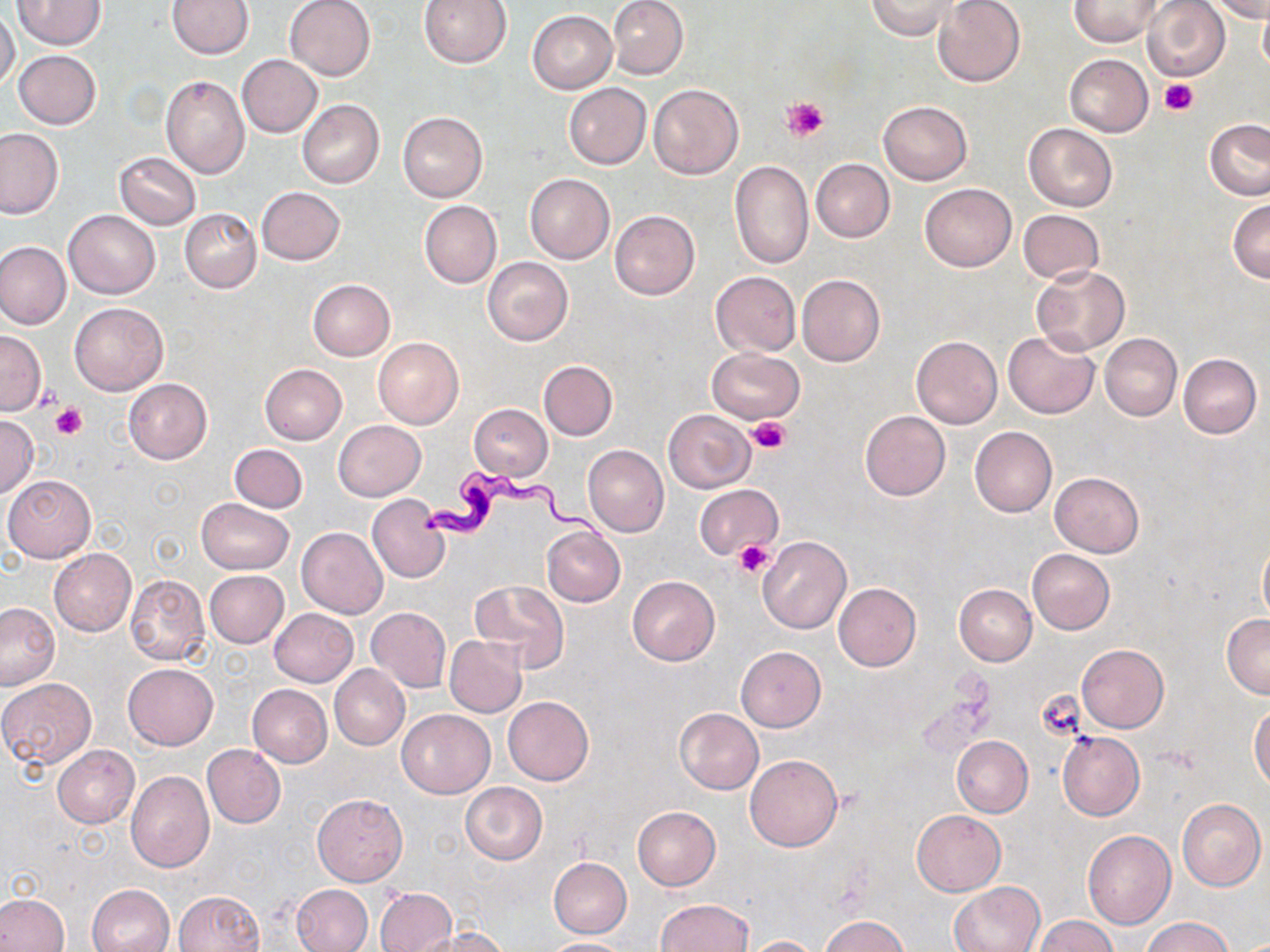

slide-level diagnosis = Trypanosoma brucei
platelet locations = approximate bounding boxes as (x1, y1, x2, y2) in pixels: (1159, 77, 1197, 117), (782, 97, 829, 141), (34, 383, 63, 412), (51, 405, 87, 440), (747, 418, 789, 453), (733, 541, 776, 578), (1036, 689, 1085, 741)
image size = 1270×952 pixels
modality = light microscopy
Trypanosoma brucei locations = approximate bounding boxes as (x1, y1, x2, y2) in pixels: (420, 468, 615, 549)
magnification = 1000x
preparation = thin blood film
stain = May-Grünwald-Giemsa
uninfected red blood cell locations = approximate bounding boxes as (x1, y1, x2, y2) in pixels: (12, 0, 104, 49), (168, 0, 254, 58), (284, 0, 376, 81), (417, 0, 512, 68), (607, 0, 688, 80), (866, 0, 958, 39), (1069, 0, 1165, 46), (1212, 0, 1270, 22), (933, 1, 1025, 88), (1142, 1, 1230, 82), (0, 8, 20, 91), (1258, 8, 1270, 75), (527, 10, 617, 94), (13, 50, 102, 129), (1064, 53, 1154, 136), (236, 55, 323, 137), (160, 75, 249, 178), (647, 82, 744, 179), (564, 83, 651, 169), (297, 99, 384, 188), (879, 100, 971, 184), (397, 111, 488, 201), (1205, 119, 1270, 198), (1023, 123, 1117, 211), (0, 129, 63, 218), (114, 151, 201, 230), (729, 159, 813, 269), (811, 159, 895, 243), (525, 173, 615, 263), (919, 182, 1017, 272), (256, 186, 344, 264), (419, 200, 502, 288), (1228, 200, 1270, 283), (180, 208, 261, 293), (63, 210, 159, 298), (610, 210, 699, 300), (1018, 210, 1105, 284), (0, 241, 72, 329), (482, 256, 573, 346), (1032, 265, 1129, 355), (710, 271, 801, 356), (796, 274, 885, 368), (308, 279, 394, 361), (69, 301, 168, 396), (0, 330, 45, 414), (1003, 331, 1100, 419), (1100, 333, 1181, 421), (911, 335, 1002, 429), (373, 337, 463, 430), (706, 348, 805, 424), (1178, 353, 1262, 438), (539, 361, 617, 440), (260, 364, 347, 444), (123, 377, 212, 464), (468, 404, 552, 480), (663, 408, 755, 493), (860, 411, 950, 500), (0, 416, 39, 497), (334, 420, 425, 500), (970, 426, 1056, 517), (229, 443, 307, 512), (582, 444, 668, 538), (1050, 471, 1144, 556), (2, 475, 95, 562), (693, 483, 782, 562), (367, 494, 450, 583), (196, 498, 292, 573), (297, 527, 389, 619), (541, 527, 625, 606), (757, 536, 851, 633), (1258, 539, 1270, 626), (49, 548, 135, 636), (1027, 549, 1114, 634), (204, 570, 289, 647), (124, 574, 209, 665), (627, 576, 719, 665), (472, 578, 569, 672), (833, 583, 921, 671), (954, 583, 1037, 665), (0, 602, 59, 692), (366, 607, 451, 692), (270, 608, 357, 686), (1222, 614, 1270, 698), (444, 636, 527, 717), (1077, 644, 1168, 732), (735, 646, 827, 732), (123, 663, 218, 750), (330, 664, 409, 749), (0, 677, 97, 769), (248, 684, 333, 767), (503, 695, 593, 786), (1249, 704, 1270, 790), (674, 707, 764, 794), (396, 710, 495, 798), (1056, 730, 1143, 820), (952, 735, 1033, 818), (202, 743, 286, 828), (52, 745, 140, 828), (744, 755, 842, 852), (126, 771, 213, 872), (460, 782, 547, 864), (312, 793, 408, 886), (1176, 799, 1266, 891), (633, 806, 720, 890), (911, 810, 1005, 895), (1082, 830, 1176, 929), (549, 857, 632, 938), (948, 881, 1045, 952), (85, 883, 175, 952), (292, 883, 373, 952), (374, 887, 456, 952), (173, 890, 264, 952), (0, 892, 69, 952), (656, 899, 753, 951), (820, 915, 911, 952), (1035, 915, 1118, 951), (1140, 916, 1233, 952), (424, 927, 508, 952), (740, 936, 823, 952), (540, 937, 633, 951)
field of view = one of a larger specimen